Assess this cell for malaria.
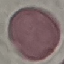
Uninfected.

Cell patch, automatically extracted from a larger field of view and resized to 64 × 64 pixels. Thin smear of blood. Giemsa-stained preparation. Acquired by smartphone through the microscope eyepiece.